Classify this cell by malaria status.
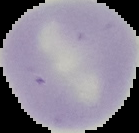
Uninfected.

Summary:
  - Image size: 139×133 pixels
  - Preparation: thin blood smear
  - Image type: segmented cell region with the area outside set to black